Locate and identify every blood parasite.
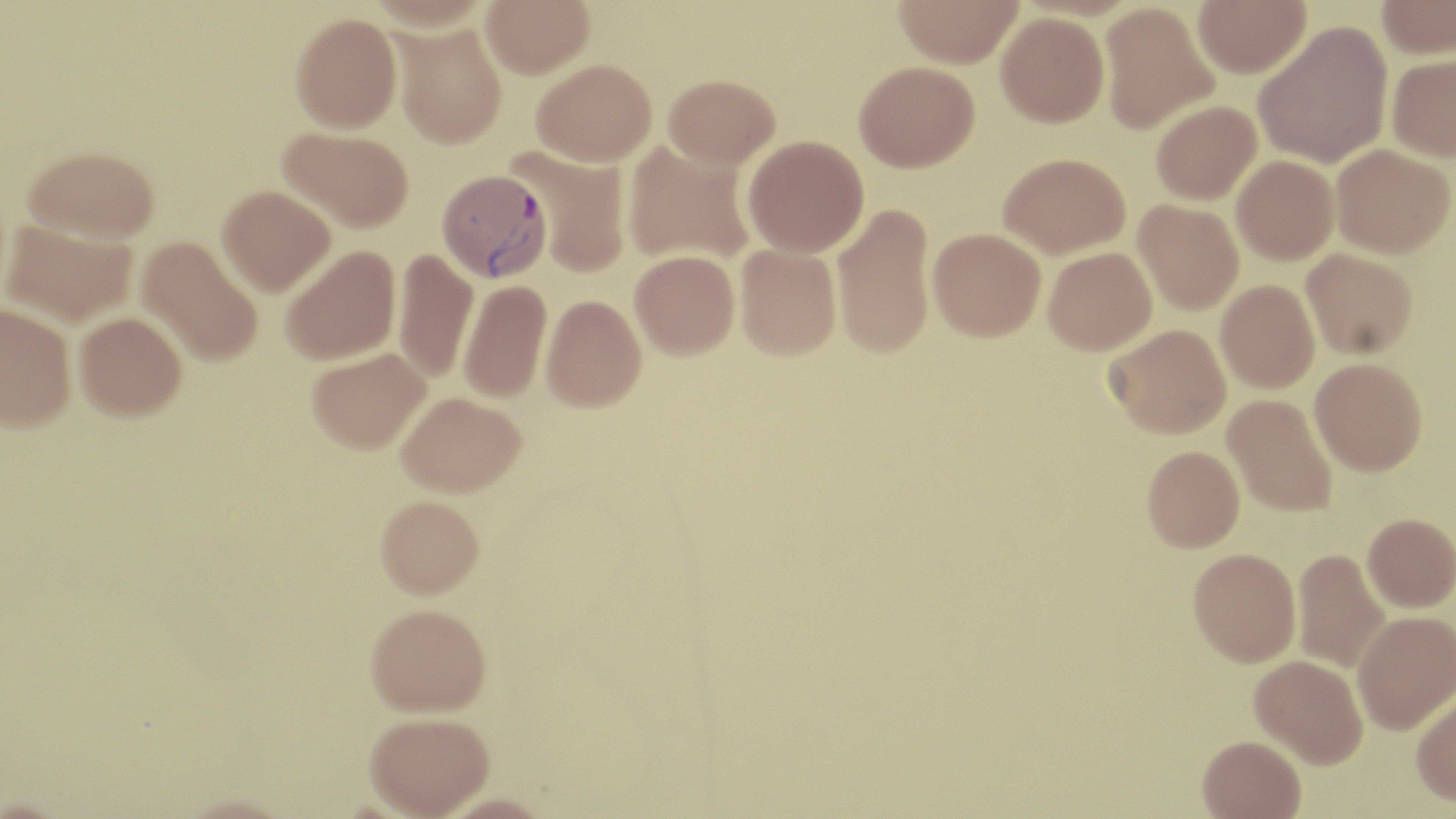
Approximate bounding boxes as (x1,y1)-(x2,y2) corner pairs in pixels.
Plasmodium vivax-infected red blood cells: (436,169)-(550,282).
No Plasmodium falciparum, Plasmodium ovale, Plasmodium malariae, Babesia divergens, or Trypanosoma brucei observed.

Uninfected red blood cell locations: (368,0)-(490,30), (481,0)-(594,78), (893,0)-(1024,68), (1192,0)-(1311,77), (1376,0)-(1456,59), (1099,3)-(1219,134), (995,12)-(1109,127), (290,13)-(401,133), (1253,20)-(1392,168), (390,23)-(508,149), (1386,54)-(1456,161), (531,58)-(656,166), (854,61)-(979,172), (663,73)-(780,168), (1151,101)-(1261,205), (277,127)-(414,232), (742,135)-(869,258), (623,141)-(755,266), (1330,144)-(1454,258), (22,145)-(160,243), (512,148)-(631,277), (999,153)-(1130,258), (1232,156)-(1339,264), (217,185)-(335,296), (1133,200)-(1244,314), (832,202)-(936,359), (2,220)-(137,327), (928,227)-(1046,341), (136,236)-(263,367), (280,244)-(400,365), (735,244)-(841,360), (392,247)-(478,384), (1043,247)-(1157,355), (1301,248)-(1417,359), (629,250)-(739,359), (458,280)-(552,403), (1215,280)-(1320,394), (541,294)-(646,412), (1,302)-(76,431), (74,312)-(187,423), (1105,324)-(1231,438), (305,348)-(431,454), (1310,357)-(1427,475), (395,391)-(526,497), (1222,394)-(1338,517), (1142,445)-(1245,552), (375,497)-(485,602), (1362,513)-(1456,612), (1188,547)-(1301,666), (1292,548)-(1391,673), (365,606)-(492,720), (1352,610)-(1455,734), (1249,654)-(1368,768), (1410,690)-(1456,807), (364,717)-(495,819), (1197,735)-(1307,818). Slide-level diagnosis: Plasmodium vivax. Light microscopy. One field of a larger specimen. May-Grünwald-Giemsa stain. Captured at 1000x magnification. Image is 1456×819 pixels. Thin blood film.